Locate every uninfected red blood cell.
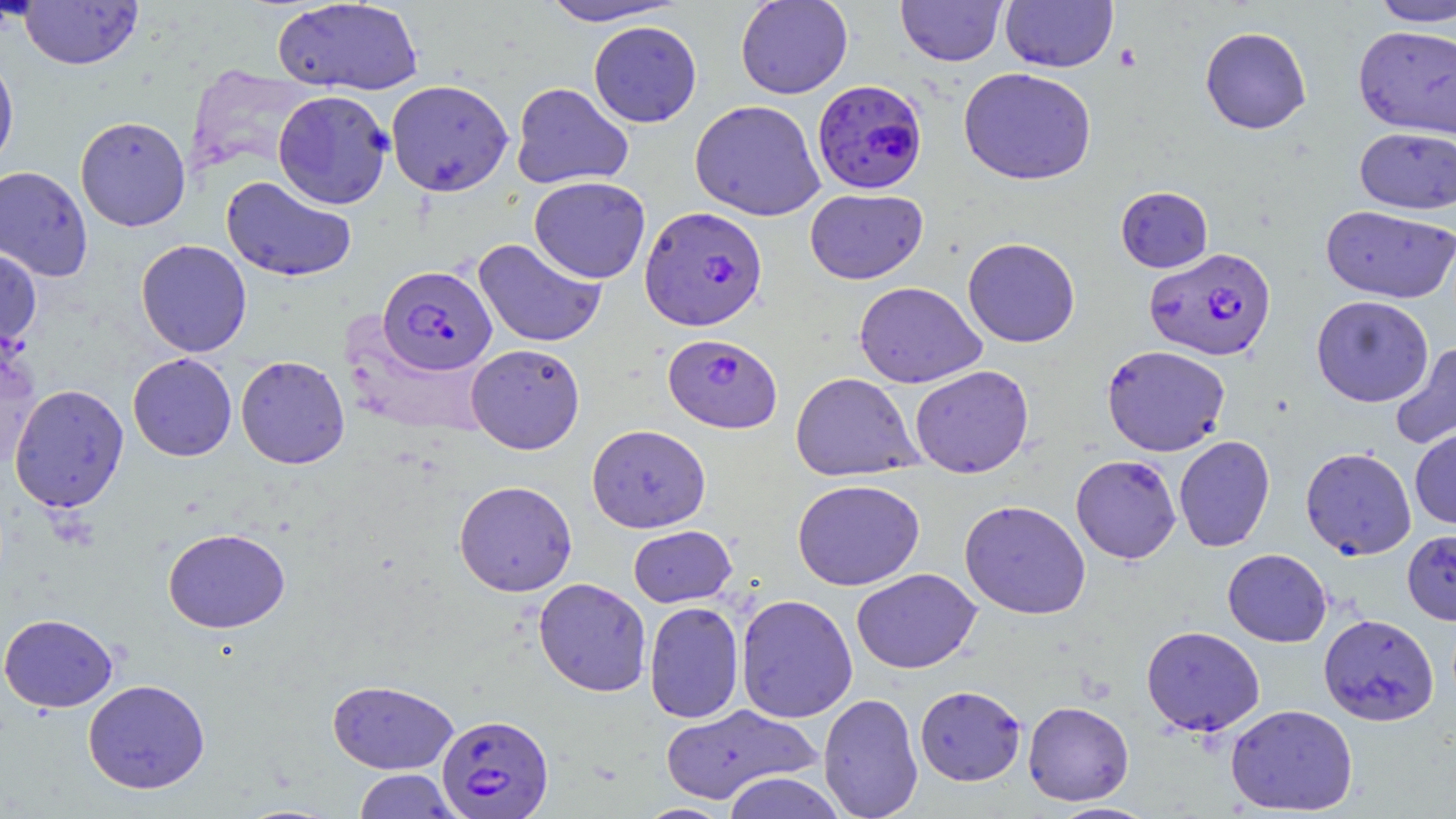

Approximate bounding boxes as (x1,y1)-(x2,y2) corner pairs in pixels.
Uninfected red blood cells: (20,0)-(143,70), (539,0)-(685,26), (735,0)-(853,99), (896,0)-(1008,66), (1000,0)-(1119,73), (1368,0)-(1456,27), (272,1)-(423,96), (588,21)-(702,127), (1353,25)-(1456,139), (1200,26)-(1312,134), (0,51)-(19,175), (958,66)-(1097,186), (385,79)-(514,196), (511,82)-(634,189), (273,90)-(393,209), (689,99)-(826,221), (75,115)-(191,232), (1355,127)-(1456,214), (0,165)-(93,282), (221,176)-(357,282), (528,176)-(651,283), (1115,186)-(1213,272), (805,188)-(928,284), (1320,205)-(1456,303), (473,237)-(607,348), (963,237)-(1081,347), (136,240)-(252,357), (0,245)-(42,352), (854,281)-(986,387), (1311,295)-(1433,407), (0,335)-(41,471), (1389,341)-(1456,452), (466,343)-(585,455), (1102,345)-(1231,456), (128,353)-(237,461), (235,355)-(350,469), (910,365)-(1034,478), (790,372)-(922,481), (9,384)-(129,512), (587,424)-(711,533), (1410,427)-(1456,529), (1174,435)-(1275,552), (1300,446)-(1416,560), (1070,454)-(1181,564), (792,478)-(925,591), (453,480)-(578,597), (959,499)-(1091,619), (628,525)-(737,607), (163,527)-(290,633), (1402,529)-(1456,625), (1222,548)-(1332,647), (851,568)-(981,673), (534,577)-(652,697), (735,594)-(858,723), (643,601)-(745,724), (0,613)-(118,712), (1319,613)-(1439,726), (1141,625)-(1265,736), (82,679)-(210,794), (327,680)-(459,774), (914,685)-(1026,786), (818,692)-(924,819), (1023,700)-(1134,806), (661,704)-(822,804), (1226,704)-(1358,815), (353,769)-(459,818), (721,772)-(847,819), (1049,801)-(1157,818), (635,803)-(735,819).

Platelet locations: (1114,44)-(1142,72). Plasmodium falciparum-infected red blood cell locations: (812,79)-(927,195), (640,205)-(767,331), (1144,248)-(1276,361), (378,265)-(497,375), (662,334)-(783,433), (436,714)-(554,818). Slide-level diagnosis: Plasmodium falciparum. Optical microscopy. Thin blood smear. May-Grünwald-Giemsa stain. Single field of view. Image is 1456×819 pixels. Captured at 1000x magnification.